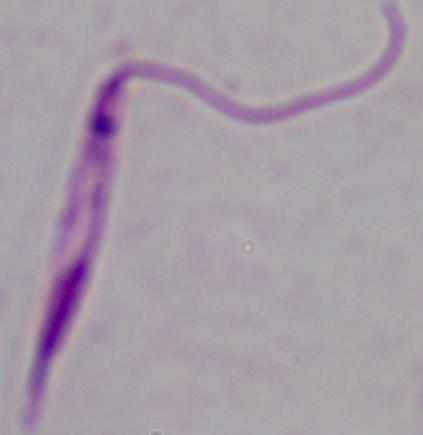
1000x magnification. Micrograph. A Leishmania parasite is seen.